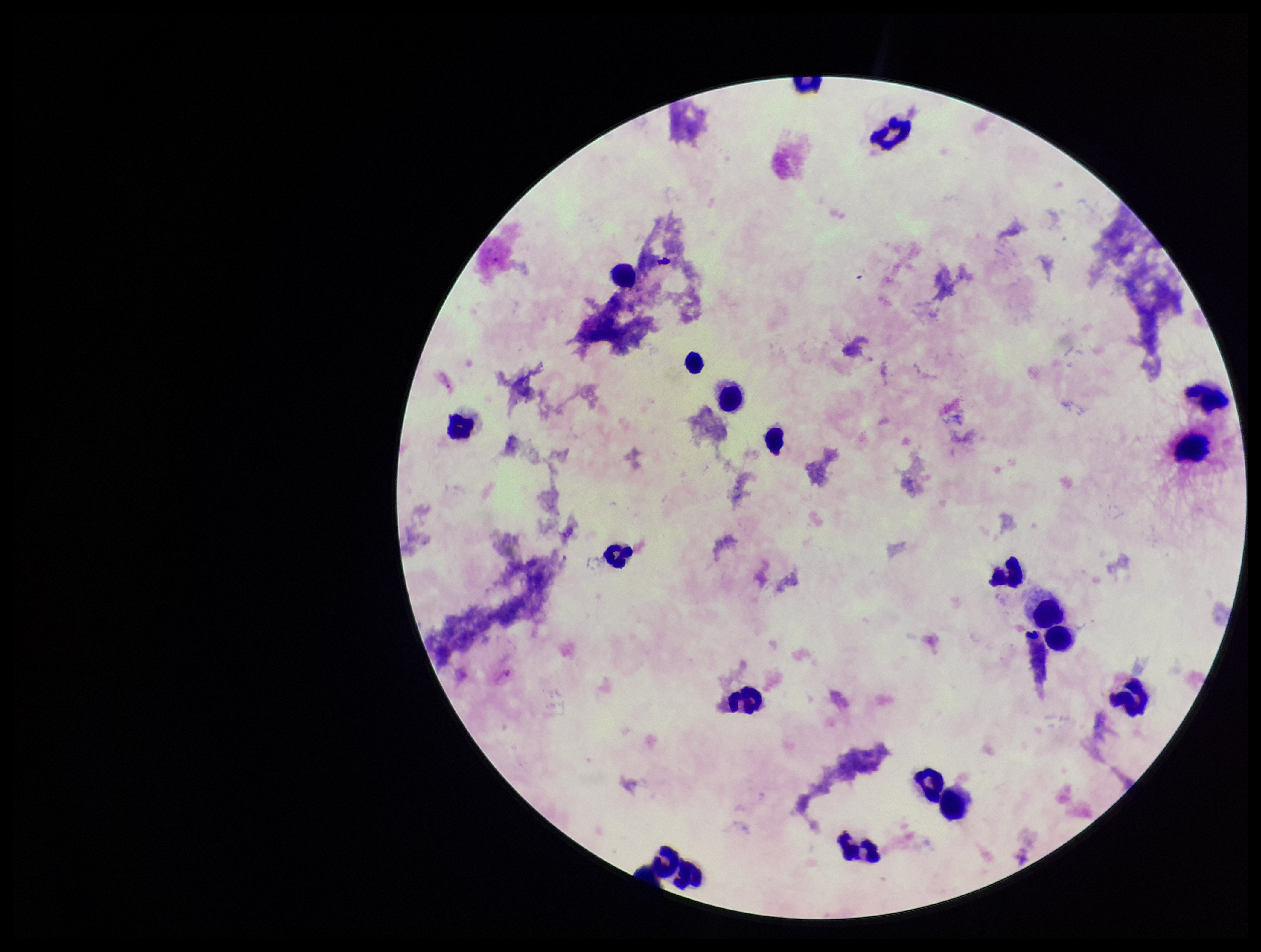

Plasmodium parasites: seen. Parasite count: 1. Species reported for this patient: Plasmodium vivax. Stained with Giemsa. Image is 1261×952 pixels. Leukocyte count: 19. Smartphone photograph taken through the eyepiece of a microscope. Patient malaria status: infected. Preparation: thick blood smear. One field from this slide.